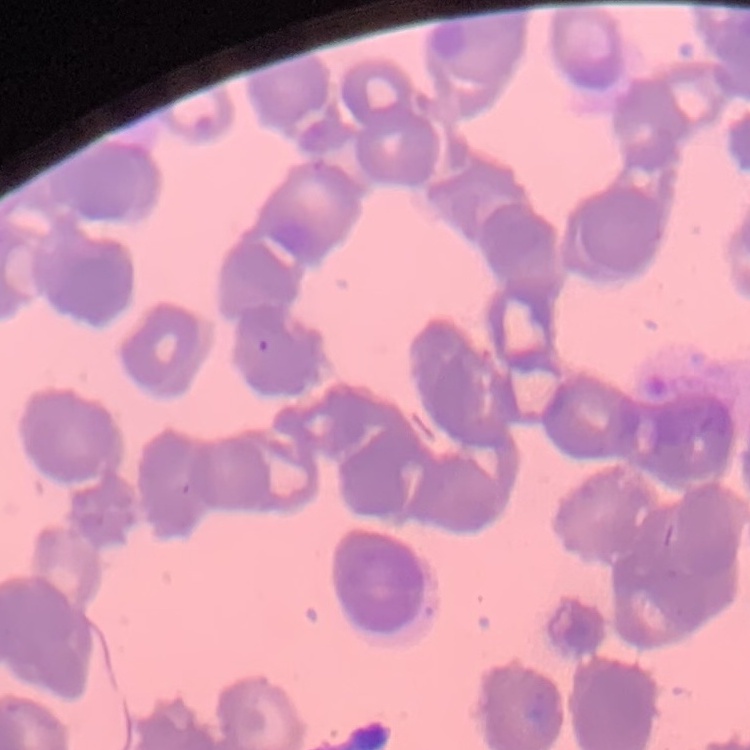
erythrocyte morphology = rouleaux formation
image type = one tile cut from a larger photomicrograph
preparation = thin blood film
stain = Field's or Giemsa